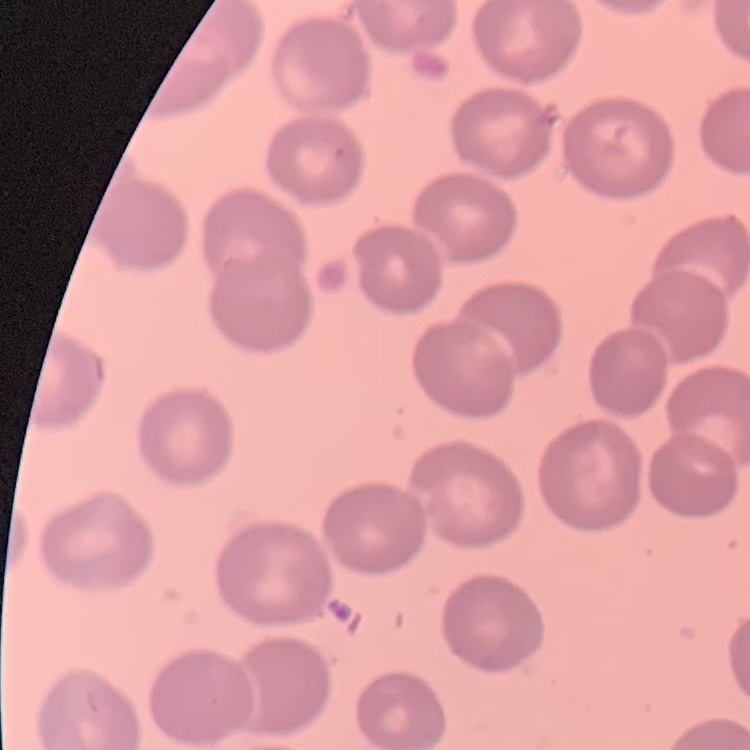

Summary:
  - Erythrocyte morphology: no rouleaux formation
  - Preparation: thin blood film
  - Image type: square crop of a larger photomicrograph
  - Stain: Field's or Giemsa